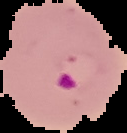
{
  "malaria_status": "parasitized",
  "image_type": "cell region segmented out of the field of view; surrounding area masked to black",
  "image_size": "127×133 pixels",
  "preparation": "thin blood film"
}